Name the parasite shown.
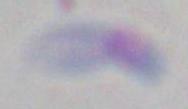
Toxoplasma gondii.

modality = photomicrograph
magnification = 1000x